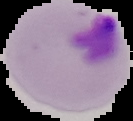
Summary:
  - Preparation: thin blood smear
  - Image size: 133×121 pixels
  - Result: malaria parasites identified
  - Image type: segmented cell region with the area outside set to black